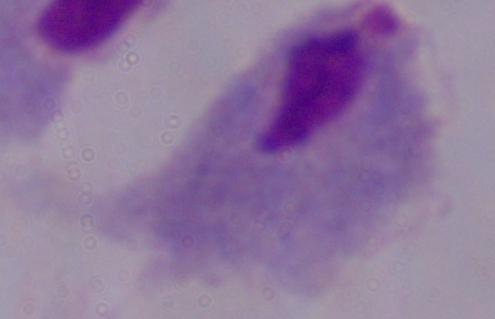
Photomicrograph. A trichomonad is seen. Captured at 1000x magnification.